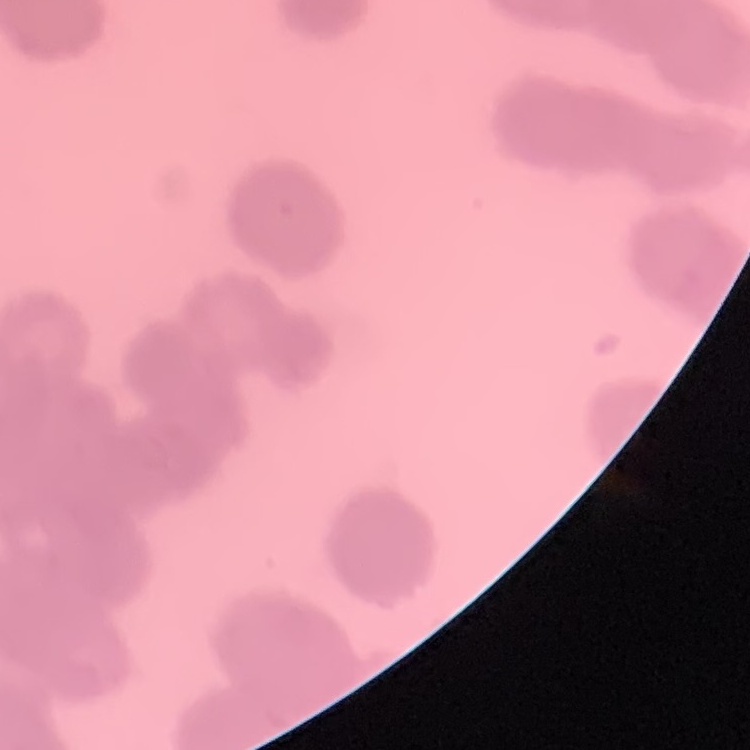

Summary:
  - Erythrocyte morphology: rouleaux formation
  - Image type: square crop of a larger photomicrograph
  - Preparation: thin blood film
  - Stain: Field's or Giemsa